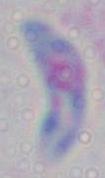

modality = micrograph
magnification = 1000x
identification = Toxoplasma gondii